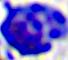
Summary:
  - Modality: micrograph
  - Magnification: 400x
  - Identification: leukocyte